Report the malaria status of this cell.
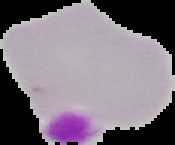

Uninfected.

Summary:
  - Preparation: thin blood film
  - Image type: segmented cell region with the area outside set to black
  - Image size: 175×145 pixels